Identify the blood parasite species.
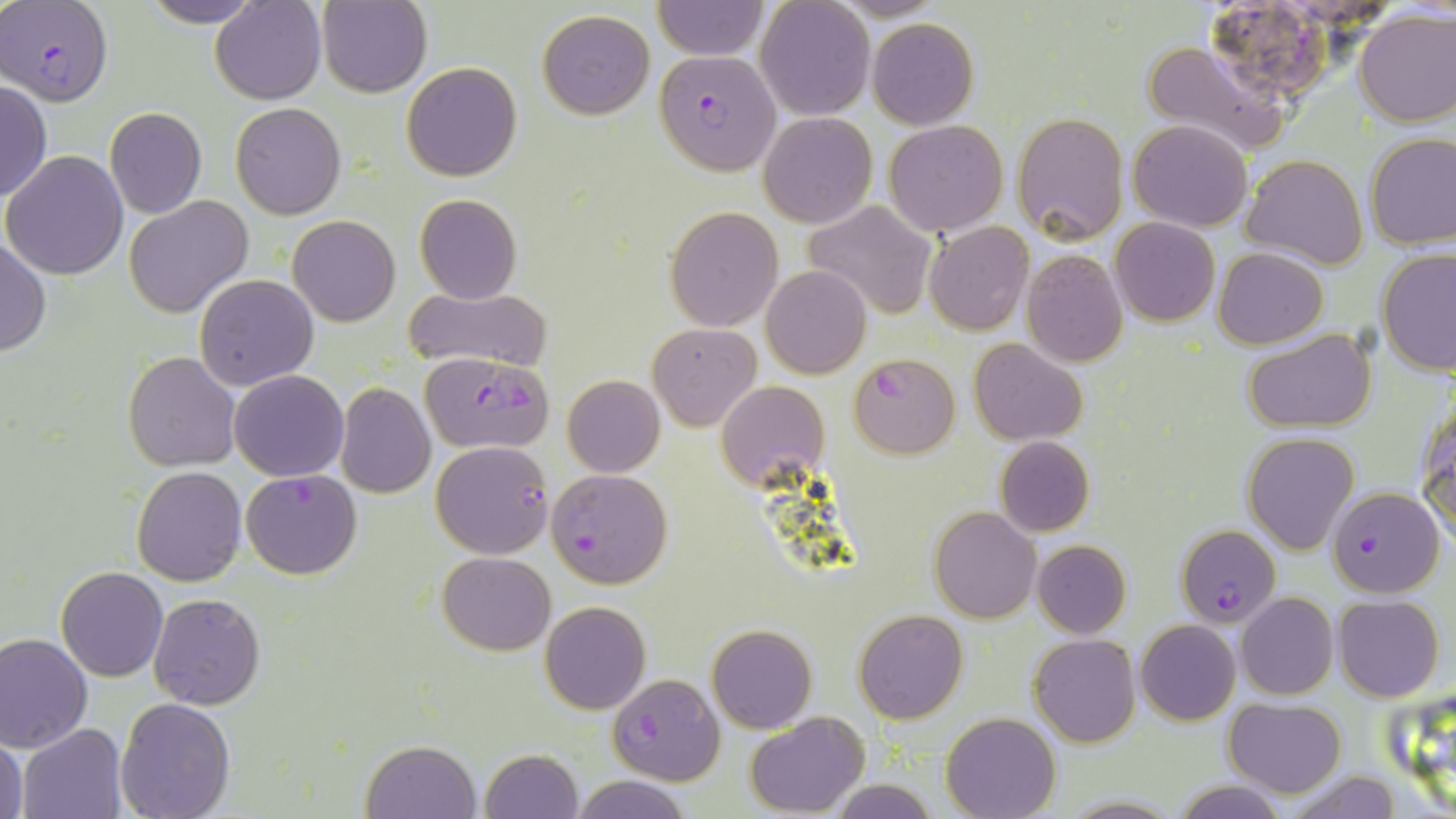

Plasmodium falciparum.

uninfected red blood cell locations = approximate bounding boxes as [x1, y1, x2, y2] in pixels: [138, 0, 266, 27], [211, 0, 326, 104], [653, 0, 768, 60], [755, 0, 875, 121], [318, 1, 432, 98], [1354, 7, 1455, 126], [536, 9, 655, 119], [867, 18, 979, 129], [1141, 39, 1287, 158], [402, 62, 523, 182], [0, 82, 51, 202], [230, 102, 345, 219], [105, 107, 206, 218], [758, 111, 877, 228], [1011, 112, 1128, 245], [1129, 119, 1253, 232], [883, 120, 1009, 236], [1364, 132, 1456, 250], [3, 151, 129, 278], [1241, 154, 1368, 271], [414, 193, 523, 304], [123, 196, 253, 318], [804, 199, 939, 319], [663, 206, 783, 330], [287, 215, 400, 326], [1110, 216, 1220, 326], [925, 222, 1033, 335], [0, 236, 50, 358], [1212, 246, 1329, 348], [1376, 247, 1455, 377], [1021, 248, 1130, 366], [760, 265, 872, 379], [194, 275, 319, 391], [402, 286, 553, 372], [648, 323, 760, 430], [1242, 329, 1377, 434], [968, 338, 1088, 444], [122, 351, 241, 471], [227, 369, 348, 480], [562, 375, 665, 477], [715, 379, 827, 489], [336, 384, 436, 498], [1418, 400, 1456, 543], [1241, 432, 1360, 553], [994, 435, 1094, 537], [132, 466, 247, 585], [930, 506, 1040, 623], [1031, 539, 1130, 639], [437, 551, 556, 656], [57, 567, 169, 682], [1237, 592, 1338, 700], [150, 593, 265, 710], [1334, 594, 1444, 701], [539, 601, 651, 714], [854, 609, 968, 723], [1135, 620, 1241, 725], [706, 625, 817, 733], [0, 633, 93, 752], [1028, 633, 1141, 747], [114, 698, 236, 818], [1224, 698, 1348, 796], [745, 711, 870, 816], [940, 713, 1062, 819], [16, 722, 128, 819], [1, 735, 28, 819], [361, 740, 482, 819], [479, 748, 584, 819], [1277, 768, 1404, 818], [570, 774, 692, 819], [830, 778, 937, 818], [1171, 780, 1289, 819], [1057, 796, 1184, 818]
field of view = single
stain = May-Grünwald-Giemsa
Plasmodium falciparum-infected red blood cell locations = approximate bounding boxes as [x1, y1, x2, y2] in pixels: [1205, 0, 1336, 108], [2, 1, 113, 105], [654, 51, 776, 172], [847, 351, 959, 457], [422, 360, 554, 447], [431, 440, 554, 559], [241, 468, 362, 579], [546, 468, 673, 588], [1328, 485, 1442, 596], [1178, 526, 1283, 625], [607, 673, 724, 784]
magnification = 1000x
image size = 1456×819 pixels
preparation = thin blood film
modality = optical microscopy